Classify this cell by malaria status.
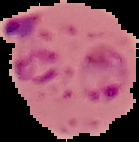
Parasitized.

preparation: thin blood smear
image_size: 139×142 pixels
image_type: segmented cell region on a black background